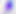 Captured at 400x magnification. Toxoplasma gondii is shown. Photomicrograph.